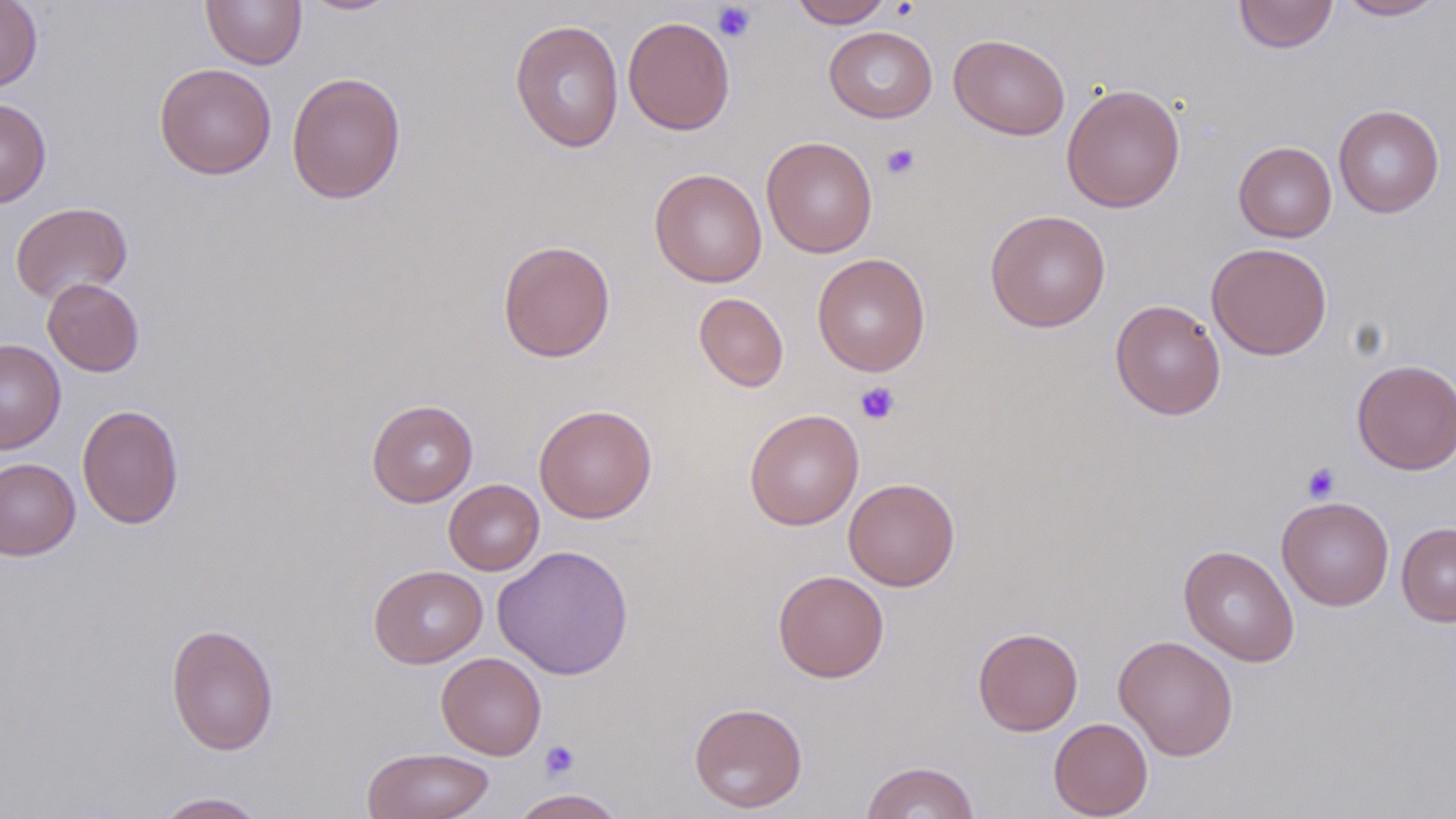
Summary:
  - Coordinate format: approximate bounding boxes as named x1/y1/x2/y2 corners in pixels
  - Platelet locations: (x1=712, y1=2, x2=757, y2=42), (x1=881, y1=143, x2=920, y2=179), (x1=855, y1=382, x2=900, y2=425), (x1=1302, y1=462, x2=1339, y2=503), (x1=540, y1=740, x2=580, y2=779)
  - Uninfected red blood cell locations: (x1=201, y1=0, x2=307, y2=69), (x1=298, y1=0, x2=402, y2=15), (x1=789, y1=0, x2=892, y2=28), (x1=1233, y1=0, x2=1339, y2=54), (x1=1335, y1=0, x2=1447, y2=21), (x1=0, y1=1, x2=42, y2=92), (x1=623, y1=15, x2=736, y2=135), (x1=510, y1=19, x2=625, y2=153), (x1=824, y1=26, x2=938, y2=123), (x1=948, y1=34, x2=1070, y2=140), (x1=154, y1=63, x2=276, y2=179), (x1=286, y1=71, x2=406, y2=204), (x1=1061, y1=83, x2=1186, y2=212), (x1=0, y1=98, x2=51, y2=207), (x1=1333, y1=104, x2=1444, y2=217), (x1=760, y1=135, x2=877, y2=258), (x1=1233, y1=141, x2=1337, y2=242), (x1=649, y1=168, x2=767, y2=287), (x1=10, y1=201, x2=133, y2=303), (x1=985, y1=210, x2=1111, y2=332), (x1=497, y1=240, x2=615, y2=362), (x1=1206, y1=242, x2=1332, y2=360), (x1=812, y1=253, x2=931, y2=377), (x1=42, y1=277, x2=145, y2=377), (x1=694, y1=292, x2=789, y2=392), (x1=1110, y1=299, x2=1226, y2=420), (x1=0, y1=338, x2=66, y2=454), (x1=1352, y1=358, x2=1456, y2=475), (x1=366, y1=399, x2=478, y2=507), (x1=77, y1=404, x2=184, y2=529), (x1=533, y1=404, x2=657, y2=523), (x1=744, y1=408, x2=864, y2=530), (x1=0, y1=457, x2=81, y2=561), (x1=843, y1=477, x2=960, y2=591), (x1=444, y1=479, x2=544, y2=575), (x1=1277, y1=496, x2=1394, y2=610), (x1=1396, y1=523, x2=1456, y2=626), (x1=493, y1=544, x2=634, y2=680), (x1=1179, y1=544, x2=1300, y2=667), (x1=369, y1=565, x2=488, y2=668), (x1=774, y1=570, x2=890, y2=682), (x1=166, y1=623, x2=279, y2=756), (x1=973, y1=627, x2=1083, y2=736), (x1=1113, y1=634, x2=1238, y2=761), (x1=436, y1=652, x2=546, y2=760), (x1=688, y1=701, x2=808, y2=813), (x1=1048, y1=717, x2=1153, y2=818), (x1=361, y1=746, x2=495, y2=819), (x1=860, y1=760, x2=980, y2=819), (x1=509, y1=788, x2=627, y2=818), (x1=151, y1=791, x2=269, y2=819)
  - Slide-level diagnosis: negative for blood parasites
  - Magnification: 1000x
  - Modality: light microscopy
  - Stain: May-Grünwald-Giemsa
  - Image size: 1456×819 pixels
  - Field of view: single
  - Preparation: thin blood smear